Report the malaria status of this cell.
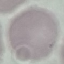
Uninfected.

Summary:
  - Capture: smartphone camera at the microscope eyepiece
  - Stain: Giemsa
  - Image type: automatically extracted cell patch, resized to 64 × 64 pixels
  - Preparation: thin smear